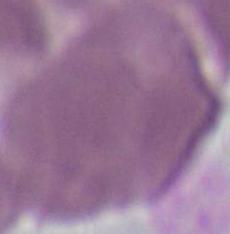
identification: red blood cell
modality: photomicrograph
magnification: 1000x